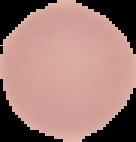

Summary:
  - Image size: 136×142 pixels
  - Preparation: thin blood film
  - Image type: segmented cell region with the area outside set to black
  - Result: no malaria parasites seen